Classify this cell by malaria status.
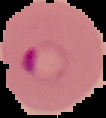
Parasitized.

Summary:
  - Preparation: thin blood smear
  - Image size: 106×118 pixels
  - Image type: segmented cell region with the area outside set to black